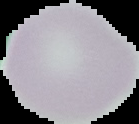 Image is 139×124 pixels. Result: no malaria parasites seen. The area outside the segmented cell region is set to black. From a thin blood film.